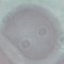
Summary:
  - Result: no malaria parasites seen
  - Image type: automatically extracted cell patch, resized to 64 × 64 pixels
  - Capture: smartphone camera at the microscope eyepiece
  - Preparation: thin blood smear
  - Stain: Giemsa